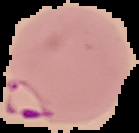

From a thin blood film. Image is 139×133 pixels. Segmented cell region on a black background. Malaria status: parasitized.